Point out each Plasmodium parasite.
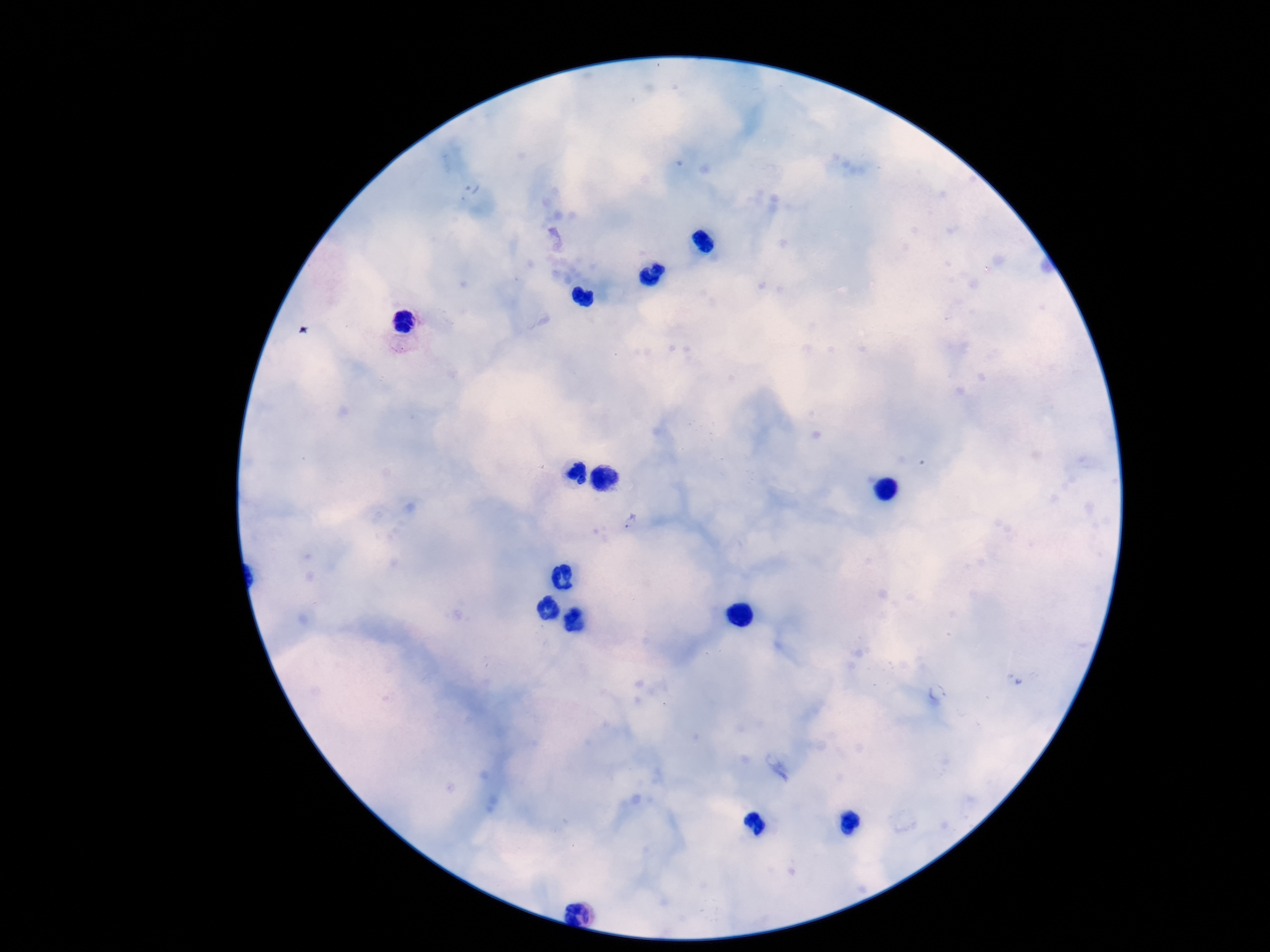
Approximate centers as (x, y) in pixels.
Plasmodium parasites: (632, 520).

Smartphone photograph taken through the microscope eyepiece. Giemsa-stained preparation. Thick blood film. Patient malaria status: positive. Image is 1270×952 pixels. 100x magnification. Single field of view.